Identify the blood parasite species.
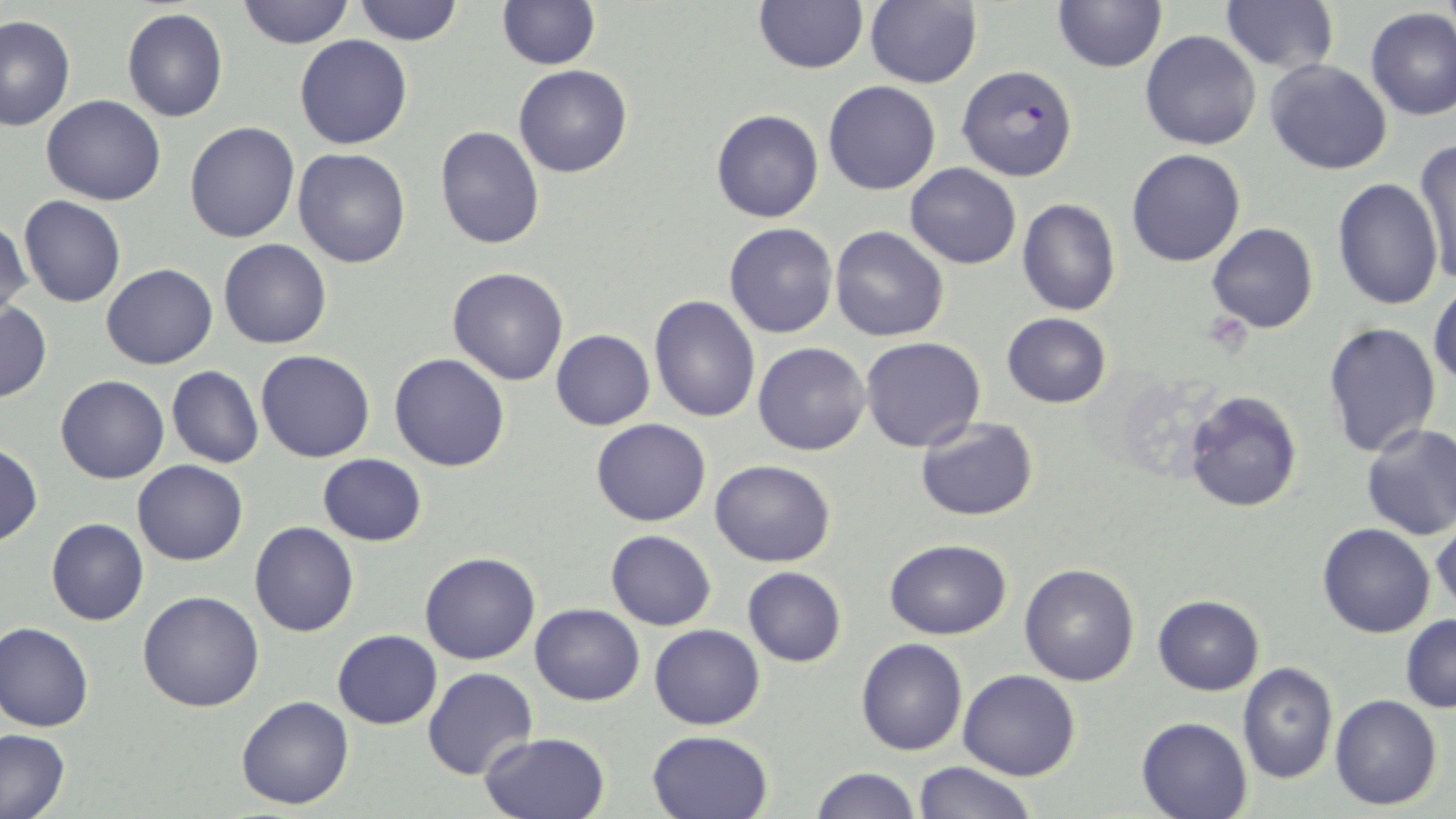

Plasmodium falciparum.

Approximate bounding boxes as named x1/y1/x2/y2 corners in pixels. Uninfected red blood cell locations: (x1=237, y1=0, x2=352, y2=49), (x1=351, y1=0, x2=466, y2=46), (x1=1051, y1=0, x2=1165, y2=72), (x1=497, y1=1, x2=600, y2=70), (x1=753, y1=1, x2=867, y2=74), (x1=863, y1=1, x2=982, y2=88), (x1=1219, y1=1, x2=1339, y2=73), (x1=1365, y1=8, x2=1456, y2=121), (x1=122, y1=9, x2=229, y2=123), (x1=1, y1=15, x2=76, y2=131), (x1=1140, y1=30, x2=1261, y2=150), (x1=294, y1=34, x2=413, y2=150), (x1=1264, y1=58, x2=1393, y2=175), (x1=515, y1=65, x2=632, y2=178), (x1=823, y1=81, x2=941, y2=196), (x1=41, y1=95, x2=165, y2=205), (x1=709, y1=95, x2=938, y2=207), (x1=711, y1=109, x2=824, y2=223), (x1=184, y1=120, x2=300, y2=242), (x1=434, y1=127, x2=545, y2=249), (x1=1411, y1=140, x2=1455, y2=287), (x1=293, y1=148, x2=412, y2=267), (x1=1126, y1=148, x2=1246, y2=268), (x1=904, y1=163, x2=1022, y2=268), (x1=1333, y1=177, x2=1442, y2=309), (x1=19, y1=196, x2=126, y2=308), (x1=1017, y1=199, x2=1120, y2=316), (x1=1, y1=219, x2=32, y2=327), (x1=723, y1=221, x2=838, y2=339), (x1=1206, y1=222, x2=1319, y2=333), (x1=828, y1=225, x2=951, y2=343), (x1=218, y1=239, x2=332, y2=350), (x1=101, y1=264, x2=218, y2=369), (x1=447, y1=267, x2=570, y2=385), (x1=1430, y1=285, x2=1456, y2=390), (x1=648, y1=296, x2=761, y2=423), (x1=0, y1=301, x2=51, y2=403), (x1=1002, y1=314, x2=1111, y2=408), (x1=1322, y1=321, x2=1442, y2=458), (x1=550, y1=329, x2=655, y2=430), (x1=860, y1=337, x2=986, y2=452), (x1=752, y1=341, x2=870, y2=456), (x1=256, y1=349, x2=374, y2=462), (x1=388, y1=353, x2=511, y2=473), (x1=167, y1=365, x2=263, y2=468), (x1=55, y1=375, x2=168, y2=484), (x1=1183, y1=389, x2=1304, y2=513), (x1=914, y1=417, x2=1039, y2=523), (x1=590, y1=418, x2=711, y2=526), (x1=1359, y1=422, x2=1456, y2=541), (x1=0, y1=442, x2=42, y2=544), (x1=317, y1=454, x2=426, y2=546), (x1=132, y1=459, x2=248, y2=565), (x1=709, y1=460, x2=837, y2=567), (x1=45, y1=517, x2=148, y2=627), (x1=1431, y1=517, x2=1455, y2=616), (x1=250, y1=522, x2=359, y2=636), (x1=1317, y1=522, x2=1435, y2=639), (x1=606, y1=530, x2=716, y2=630), (x1=884, y1=538, x2=1012, y2=639), (x1=419, y1=551, x2=540, y2=665), (x1=1019, y1=563, x2=1140, y2=686), (x1=742, y1=567, x2=847, y2=667), (x1=138, y1=590, x2=266, y2=712), (x1=1151, y1=595, x2=1264, y2=695), (x1=530, y1=604, x2=644, y2=705), (x1=1399, y1=615, x2=1456, y2=711), (x1=1, y1=623, x2=95, y2=733), (x1=649, y1=624, x2=765, y2=730), (x1=331, y1=630, x2=442, y2=729), (x1=856, y1=638, x2=969, y2=756), (x1=1238, y1=664, x2=1338, y2=784), (x1=424, y1=668, x2=537, y2=780), (x1=958, y1=670, x2=1081, y2=780), (x1=236, y1=695, x2=354, y2=810), (x1=1330, y1=695, x2=1442, y2=810), (x1=1136, y1=715, x2=1254, y2=819), (x1=1, y1=729, x2=69, y2=818), (x1=647, y1=729, x2=773, y2=818), (x1=478, y1=731, x2=610, y2=819), (x1=913, y1=760, x2=1037, y2=819), (x1=810, y1=767, x2=921, y2=819). Plasmodium falciparum-infected red blood cell locations: (x1=956, y1=65, x2=1079, y2=182). Light microscopy. Image is 1456×819 pixels. Thin blood smear. 1000x magnification. One field of a larger specimen. May-Grünwald-Giemsa-stained preparation.